Give the extent of all Plasmodium vivax-infected red blood cells.
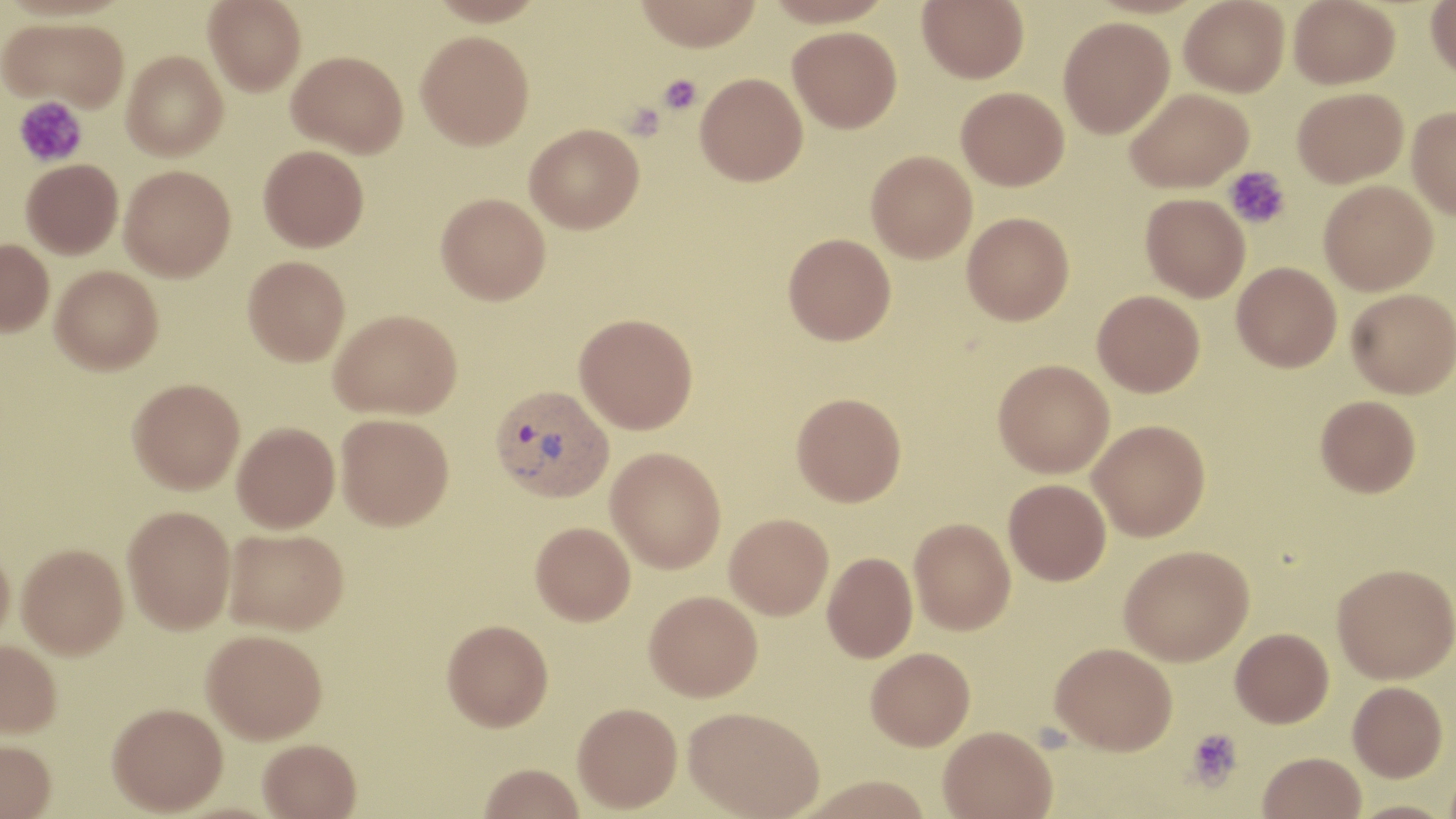
Approximate bounding boxes as [x1, y1, x2, y2] in pixels.
Plasmodium vivax-infected red blood cells: [490, 384, 614, 501].

Summary:
  - Platelet locations: [657, 74, 702, 116], [13, 97, 87, 167], [1223, 165, 1291, 229], [1185, 727, 1243, 791]
  - Uninfected red blood cell locations: [204, 0, 306, 96], [633, 0, 763, 51], [764, 0, 896, 27], [917, 0, 1028, 83], [1179, 0, 1289, 97], [1288, 0, 1400, 88], [1426, 0, 1456, 79], [1, 16, 130, 112], [1058, 17, 1174, 138], [788, 26, 902, 133], [416, 30, 534, 150], [122, 50, 228, 160], [287, 50, 408, 157], [695, 72, 808, 186], [956, 86, 1069, 190], [1126, 87, 1253, 193], [1292, 87, 1408, 187], [1407, 106, 1456, 218], [524, 123, 644, 233], [258, 145, 369, 251], [866, 150, 977, 263], [21, 159, 123, 259], [119, 164, 236, 280], [1319, 179, 1438, 295], [436, 193, 550, 304], [1141, 193, 1250, 301], [962, 212, 1074, 325], [783, 233, 896, 345], [0, 238, 54, 336], [243, 255, 350, 366], [1232, 261, 1341, 372], [50, 265, 163, 374], [1346, 288, 1456, 398], [1093, 290, 1205, 396], [329, 309, 461, 419], [574, 313, 698, 433], [993, 359, 1114, 478], [128, 378, 245, 493], [791, 392, 906, 506], [1316, 395, 1420, 497], [336, 413, 454, 530], [1088, 420, 1210, 541], [232, 422, 340, 532], [606, 447, 726, 573], [1004, 479, 1111, 585], [123, 505, 236, 633], [724, 513, 833, 620], [909, 517, 1015, 634], [530, 522, 635, 625], [224, 528, 348, 634], [17, 543, 128, 658], [1119, 544, 1253, 665], [0, 545, 15, 648], [822, 552, 917, 662], [1333, 563, 1456, 683], [644, 590, 762, 701], [442, 619, 553, 731], [1230, 628, 1334, 727], [202, 629, 327, 744], [0, 640, 61, 738], [1050, 641, 1177, 754], [866, 647, 975, 750], [1348, 681, 1447, 781], [572, 702, 682, 813], [108, 703, 228, 815], [684, 706, 824, 818], [938, 725, 1057, 818], [258, 739, 361, 818], [0, 740, 56, 819], [1258, 752, 1366, 819], [478, 763, 585, 819], [798, 775, 933, 819], [1345, 800, 1456, 819]
  - Slide-level diagnosis: Plasmodium vivax
  - Modality: light microscopy
  - Magnification: 1000x
  - Preparation: thin blood smear
  - Field of view: single
  - Image size: 1456×819 pixels
  - Stain: May-Grünwald-Giemsa